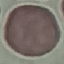
Result: no malaria parasites seen. Cell patch, automatically extracted from a larger field of view and resized to 64 × 64 pixels. Giemsa-stained preparation. Thin blood smear. Acquired by smartphone through the microscope eyepiece.